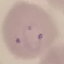 Malaria status: parasitized. Cell patch, automatically extracted from a larger field of view and resized to 64 × 64 pixels. Acquired by smartphone through the microscope eyepiece. Giemsa-stained preparation. Thin smear of blood.